State the blood parasite species.
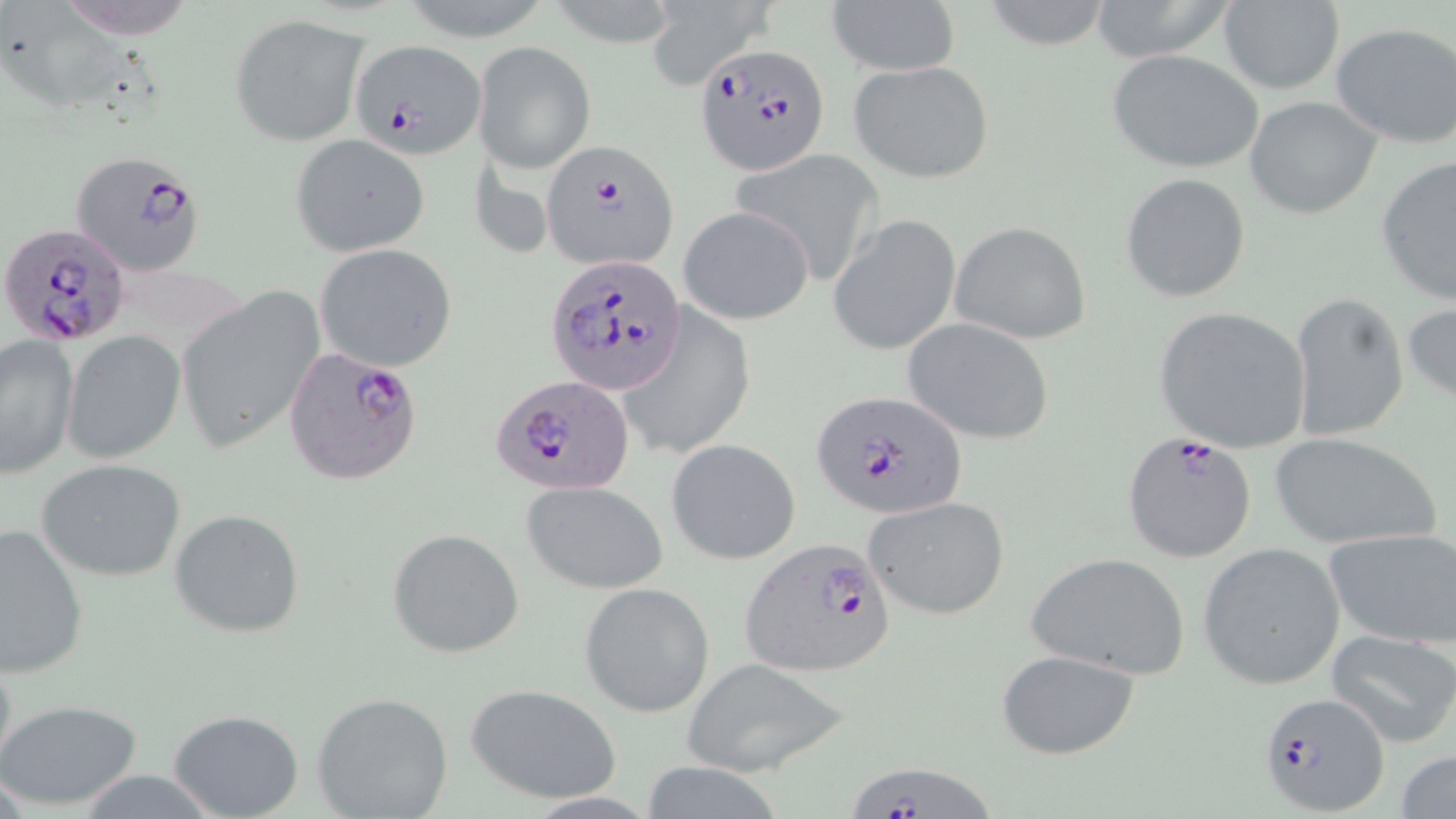

Plasmodium falciparum.

image size = 1456×819 pixels
magnification = 1000x
stain = May-Grünwald-Giemsa
modality = light microscopy
uninfected red blood cell locations = approximate bounding boxes as [x1, y1, x2, y2] in pixels: [1085, 0, 1240, 62], [977, 1, 1117, 51], [1216, 1, 1345, 95], [824, 2, 959, 77], [644, 3, 776, 89], [230, 15, 371, 145], [1329, 22, 1456, 149], [473, 41, 595, 173], [1105, 49, 1266, 174], [846, 59, 996, 185], [1245, 96, 1382, 219], [290, 133, 429, 256], [731, 146, 883, 283], [1376, 154, 1456, 304], [1121, 172, 1252, 304], [679, 205, 815, 325], [830, 215, 962, 355], [949, 221, 1092, 345], [315, 244, 458, 373], [177, 287, 324, 455], [1288, 291, 1410, 443], [1403, 298, 1456, 411], [616, 307, 755, 462], [1153, 307, 1312, 453], [902, 317, 1056, 446], [61, 330, 185, 465], [1, 335, 78, 478], [1264, 432, 1445, 550], [667, 439, 801, 565], [36, 458, 187, 581], [4, 468, 144, 642], [520, 480, 667, 595], [863, 495, 1011, 622], [169, 508, 305, 638], [0, 523, 90, 677], [387, 528, 524, 658], [1325, 528, 1456, 647], [1198, 542, 1347, 690], [1026, 552, 1191, 679], [578, 582, 715, 716], [1326, 630, 1456, 749], [995, 651, 1141, 759], [678, 658, 849, 776], [464, 682, 624, 804], [312, 692, 453, 819], [0, 698, 142, 810], [170, 710, 305, 819], [1395, 747, 1456, 819]
field of view = one of a larger specimen
preparation = thin blood film
Plasmodium falciparum-infected red blood cell locations = approximate bounding boxes as [x1, y1, x2, y2] in pixels: [351, 38, 486, 157], [693, 42, 833, 176], [542, 141, 678, 272], [69, 148, 208, 278], [0, 224, 132, 345], [549, 253, 687, 396], [283, 345, 426, 487], [494, 378, 635, 494], [812, 389, 965, 522], [1122, 432, 1257, 562], [739, 537, 898, 678], [1257, 692, 1390, 814], [851, 767, 999, 819]